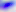

Summary:
  - Modality: photomicrograph
  - Magnification: 400x
  - Identification: Toxoplasma gondii